Give the extent of all Plasmodium falciparum-infected red blood cells.
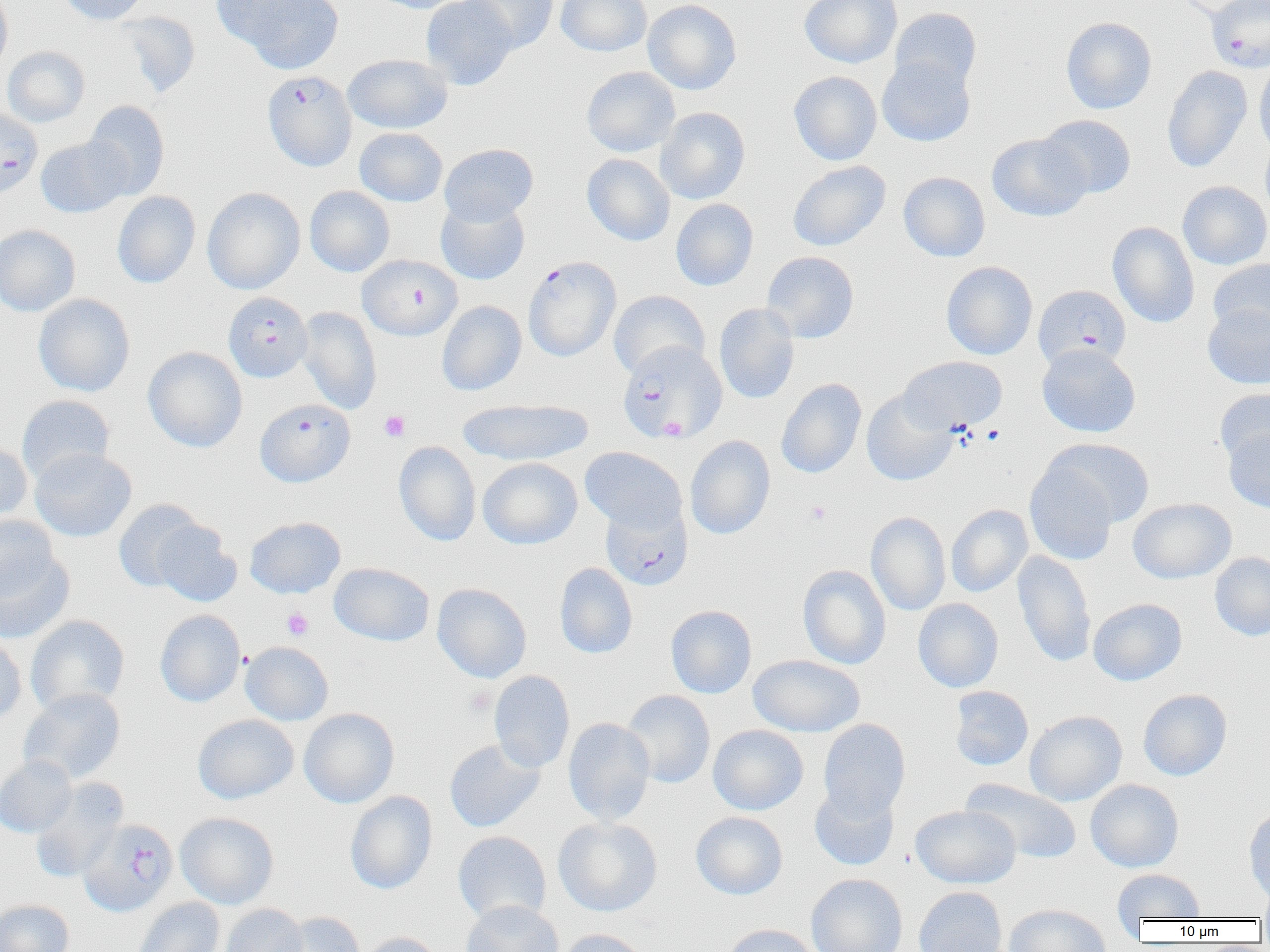

Approximate bounding boxes as named x1/y1/x2/y2 corners in pixels.
Plasmodium falciparum-infected red blood cells: (x1=1206, y1=0, x2=1270, y2=74), (x1=263, y1=70, x2=356, y2=171), (x1=0, y1=108, x2=43, y2=199), (x1=357, y1=255, x2=463, y2=340), (x1=523, y1=255, x2=620, y2=361), (x1=1033, y1=285, x2=1131, y2=372), (x1=223, y1=292, x2=312, y2=382), (x1=617, y1=341, x2=727, y2=444), (x1=255, y1=398, x2=355, y2=487), (x1=600, y1=502, x2=692, y2=590), (x1=79, y1=818, x2=178, y2=916).

Platelet locations: (x1=379, y1=410, x2=410, y2=442), (x1=805, y1=501, x2=831, y2=525), (x1=281, y1=608, x2=314, y2=640), (x1=465, y1=686, x2=496, y2=716). Uninfected red blood cell locations: (x1=56, y1=0, x2=148, y2=25), (x1=224, y1=0, x2=345, y2=74), (x1=369, y1=0, x2=470, y2=13), (x1=421, y1=0, x2=518, y2=90), (x1=464, y1=0, x2=558, y2=52), (x1=556, y1=0, x2=652, y2=57), (x1=643, y1=0, x2=741, y2=94), (x1=800, y1=0, x2=902, y2=68), (x1=1178, y1=0, x2=1263, y2=21), (x1=0, y1=1, x2=13, y2=75), (x1=889, y1=7, x2=982, y2=93), (x1=116, y1=11, x2=200, y2=97), (x1=1061, y1=17, x2=1157, y2=114), (x1=2, y1=46, x2=90, y2=127), (x1=342, y1=54, x2=453, y2=134), (x1=877, y1=56, x2=975, y2=147), (x1=1254, y1=59, x2=1270, y2=160), (x1=582, y1=66, x2=680, y2=157), (x1=1162, y1=66, x2=1253, y2=173), (x1=789, y1=71, x2=881, y2=165), (x1=84, y1=100, x2=170, y2=199), (x1=655, y1=107, x2=750, y2=204), (x1=1038, y1=115, x2=1136, y2=199), (x1=354, y1=128, x2=448, y2=207), (x1=986, y1=133, x2=1091, y2=221), (x1=1260, y1=134, x2=1270, y2=224), (x1=36, y1=136, x2=131, y2=218), (x1=439, y1=143, x2=538, y2=226), (x1=582, y1=153, x2=675, y2=246), (x1=788, y1=161, x2=890, y2=251), (x1=898, y1=172, x2=990, y2=261), (x1=1177, y1=181, x2=1270, y2=270), (x1=304, y1=186, x2=394, y2=277), (x1=202, y1=187, x2=305, y2=294), (x1=112, y1=191, x2=201, y2=288), (x1=435, y1=198, x2=530, y2=284), (x1=671, y1=199, x2=759, y2=290), (x1=1108, y1=222, x2=1199, y2=328), (x1=0, y1=224, x2=80, y2=317), (x1=761, y1=251, x2=859, y2=344), (x1=1208, y1=259, x2=1270, y2=339), (x1=941, y1=261, x2=1038, y2=360), (x1=608, y1=290, x2=709, y2=379), (x1=34, y1=294, x2=135, y2=397), (x1=437, y1=301, x2=527, y2=395), (x1=714, y1=303, x2=799, y2=404), (x1=1203, y1=304, x2=1270, y2=389), (x1=297, y1=306, x2=382, y2=415), (x1=1037, y1=344, x2=1141, y2=438), (x1=143, y1=346, x2=247, y2=452), (x1=897, y1=356, x2=1007, y2=433), (x1=777, y1=378, x2=866, y2=478), (x1=1215, y1=388, x2=1270, y2=474), (x1=861, y1=390, x2=958, y2=486), (x1=17, y1=395, x2=114, y2=484), (x1=458, y1=398, x2=593, y2=466), (x1=1221, y1=422, x2=1270, y2=514), (x1=685, y1=435, x2=775, y2=539), (x1=1045, y1=438, x2=1155, y2=529), (x1=0, y1=441, x2=33, y2=521), (x1=393, y1=441, x2=481, y2=546), (x1=580, y1=447, x2=686, y2=533), (x1=30, y1=448, x2=137, y2=542), (x1=478, y1=457, x2=582, y2=549), (x1=1025, y1=460, x2=1118, y2=565), (x1=1128, y1=497, x2=1236, y2=583), (x1=113, y1=498, x2=207, y2=592), (x1=946, y1=504, x2=1033, y2=597), (x1=866, y1=512, x2=951, y2=615), (x1=0, y1=514, x2=59, y2=600), (x1=245, y1=516, x2=345, y2=598), (x1=151, y1=520, x2=241, y2=607), (x1=1013, y1=550, x2=1096, y2=667), (x1=0, y1=551, x2=75, y2=643), (x1=1209, y1=552, x2=1270, y2=640), (x1=329, y1=563, x2=434, y2=646), (x1=555, y1=563, x2=638, y2=659), (x1=798, y1=564, x2=891, y2=669), (x1=432, y1=583, x2=532, y2=683), (x1=913, y1=598, x2=1004, y2=692), (x1=1088, y1=598, x2=1187, y2=686), (x1=665, y1=605, x2=757, y2=698), (x1=155, y1=609, x2=245, y2=707), (x1=25, y1=614, x2=129, y2=715), (x1=0, y1=634, x2=27, y2=726), (x1=241, y1=642, x2=334, y2=725), (x1=748, y1=654, x2=865, y2=737), (x1=489, y1=670, x2=575, y2=773), (x1=949, y1=686, x2=1034, y2=771), (x1=19, y1=688, x2=126, y2=784), (x1=1138, y1=689, x2=1232, y2=781), (x1=621, y1=690, x2=715, y2=788), (x1=298, y1=708, x2=399, y2=808), (x1=1025, y1=710, x2=1127, y2=806), (x1=193, y1=714, x2=299, y2=804), (x1=563, y1=718, x2=655, y2=825), (x1=818, y1=719, x2=911, y2=820), (x1=708, y1=724, x2=808, y2=815), (x1=444, y1=739, x2=545, y2=833), (x1=0, y1=756, x2=77, y2=838), (x1=30, y1=778, x2=128, y2=882), (x1=961, y1=778, x2=1082, y2=864), (x1=1085, y1=779, x2=1184, y2=872), (x1=810, y1=783, x2=900, y2=871), (x1=345, y1=791, x2=438, y2=894), (x1=910, y1=805, x2=1021, y2=888), (x1=1243, y1=807, x2=1270, y2=905), (x1=690, y1=811, x2=788, y2=900), (x1=175, y1=812, x2=279, y2=909), (x1=553, y1=816, x2=663, y2=916), (x1=453, y1=831, x2=551, y2=924), (x1=1112, y1=869, x2=1205, y2=921), (x1=806, y1=874, x2=907, y2=952), (x1=1256, y1=883, x2=1270, y2=921), (x1=913, y1=886, x2=1008, y2=952), (x1=132, y1=897, x2=225, y2=952), (x1=0, y1=899, x2=74, y2=952), (x1=461, y1=899, x2=564, y2=952), (x1=220, y1=903, x2=308, y2=952), (x1=1004, y1=903, x2=1112, y2=952), (x1=275, y1=912, x2=364, y2=952), (x1=720, y1=924, x2=819, y2=952), (x1=556, y1=928, x2=653, y2=952), (x1=358, y1=932, x2=446, y2=952). Slide-level diagnosis: Plasmodium falciparum. Optical microscopy. Thin blood smear. 1000x magnification. Image is 1270×952 pixels. One field of a larger specimen.